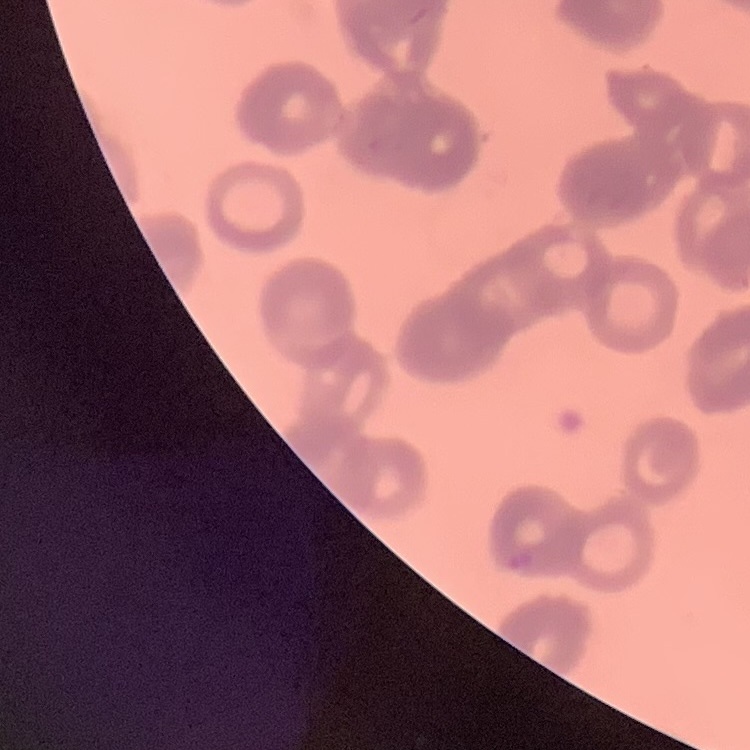
Summary:
  - Red blood cell morphology: rouleaux formation
  - Image type: square crop of a larger photomicrograph
  - Preparation: thin blood smear
  - Stain: Field's or Giemsa